Report the malaria status of this cell.
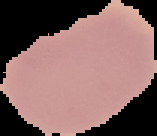

It is uninfected.

From a thin blood film. Image is 157×136 pixels. The area outside the segmented cell region is set to black.